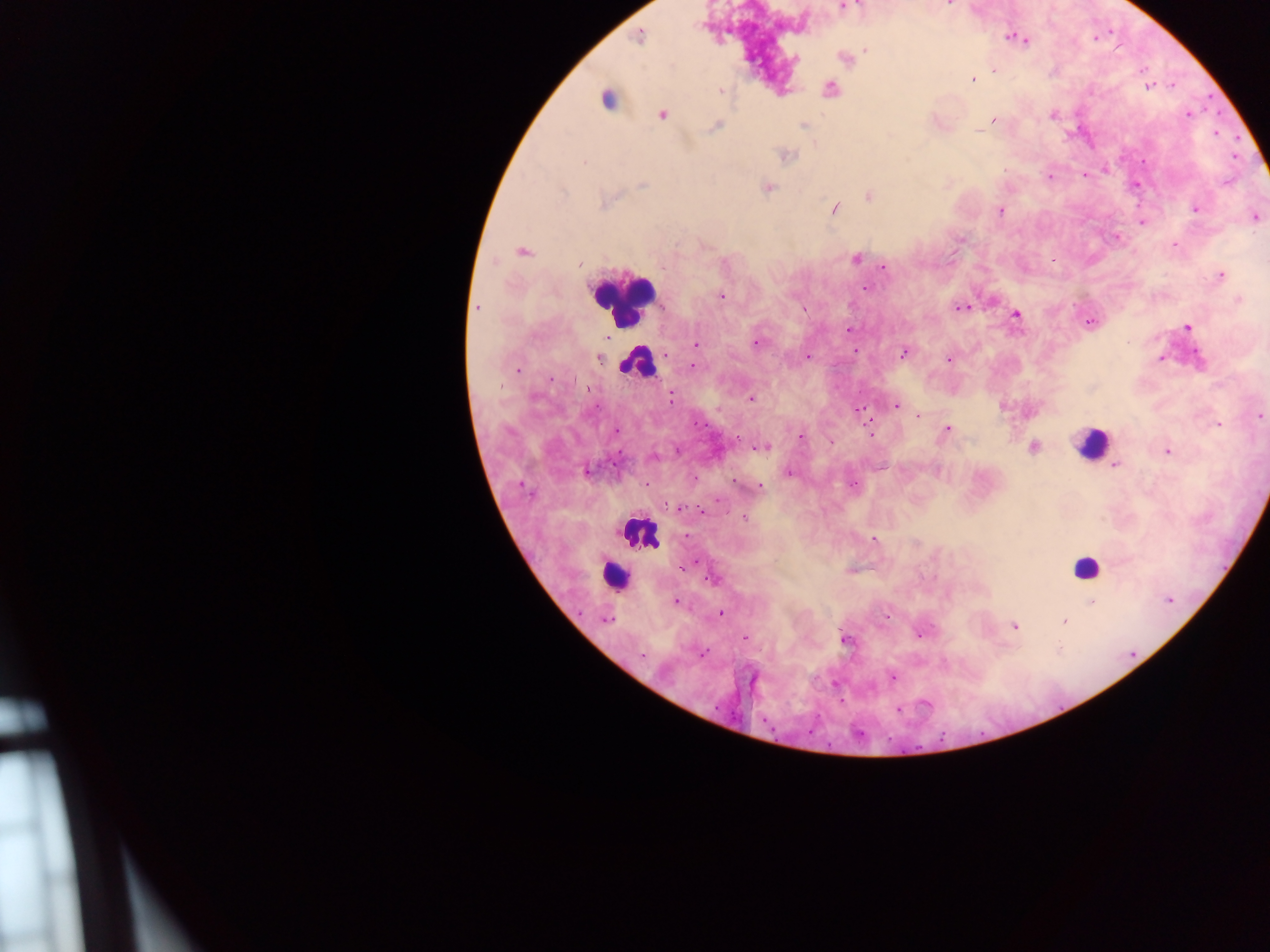

Approximate centers as (x, y) in pixels.
Summary:
  - Malaria parasite locations: (949, 5), (843, 7), (638, 35), (1010, 37), (1094, 38), (1020, 39), (1025, 39), (866, 51), (844, 57), (794, 59), (994, 69), (973, 79), (1172, 85), (1147, 86), (829, 90), (719, 91), (607, 98), (662, 113), (1187, 114), (1053, 115), (994, 121), (715, 125), (977, 131), (1216, 133), (786, 154), (1105, 169), (1083, 175), (1050, 176), (1135, 185), (766, 187), (869, 195), (834, 208), (1194, 208), (1001, 211), (1254, 216), (1141, 222), (1115, 236), (1174, 246), (521, 252), (855, 258), (580, 263), (883, 265), (1220, 275), (865, 288), (720, 296), (1239, 298), (477, 307), (961, 307), (1016, 314), (1090, 322), (1186, 327), (848, 329), (757, 343), (695, 345), (854, 351), (903, 352), (808, 356), (599, 357), (1160, 358), (948, 359), (692, 366), (517, 369), (750, 399), (895, 405), (1003, 406), (857, 409), (1029, 412), (918, 416), (1259, 416), (1217, 424), (947, 429), (615, 431), (871, 432), (800, 437), (831, 440), (761, 447), (1034, 447), (1167, 450), (652, 457), (1114, 465), (586, 470), (937, 471), (788, 472), (734, 481), (853, 485), (759, 486), (678, 507), (745, 518), (873, 539), (683, 566), (712, 579), (1169, 600), (676, 601), (1091, 602), (719, 613), (887, 615), (606, 620), (1064, 621), (1014, 626), (918, 632), (745, 638), (844, 639), (702, 652), (891, 676), (925, 704), (898, 709)
  - Leukocyte locations: (621, 297), (636, 362), (1091, 444), (639, 532), (1085, 568), (614, 575)
  - Capture: mobile-phone photograph through a microscope
  - Image size: 1270×952 pixels
  - Field of view: single
  - Preparation: thick blood film
  - Country: Ghana